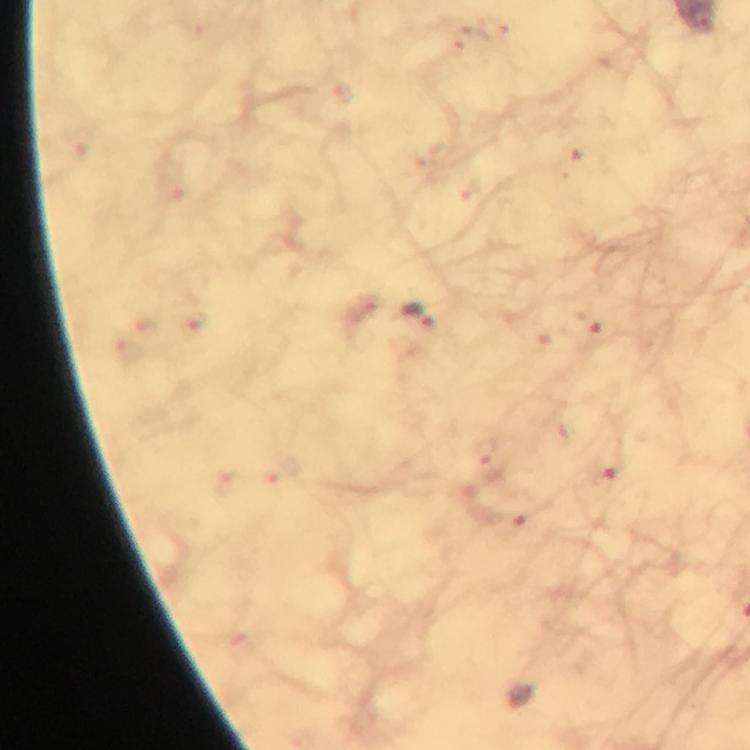 Approximate object centers, in pixels from the top-left corner. Malaria parasite locations: (x=421, y=318). From a diagnostic examination for malaria. At 100x magnification. Image is 750×750 pixels. Photographed with a smartphone mounted on the microscope. A crop from one field of view. Thick blood film. Giemsa stain. Immersion oil applied.